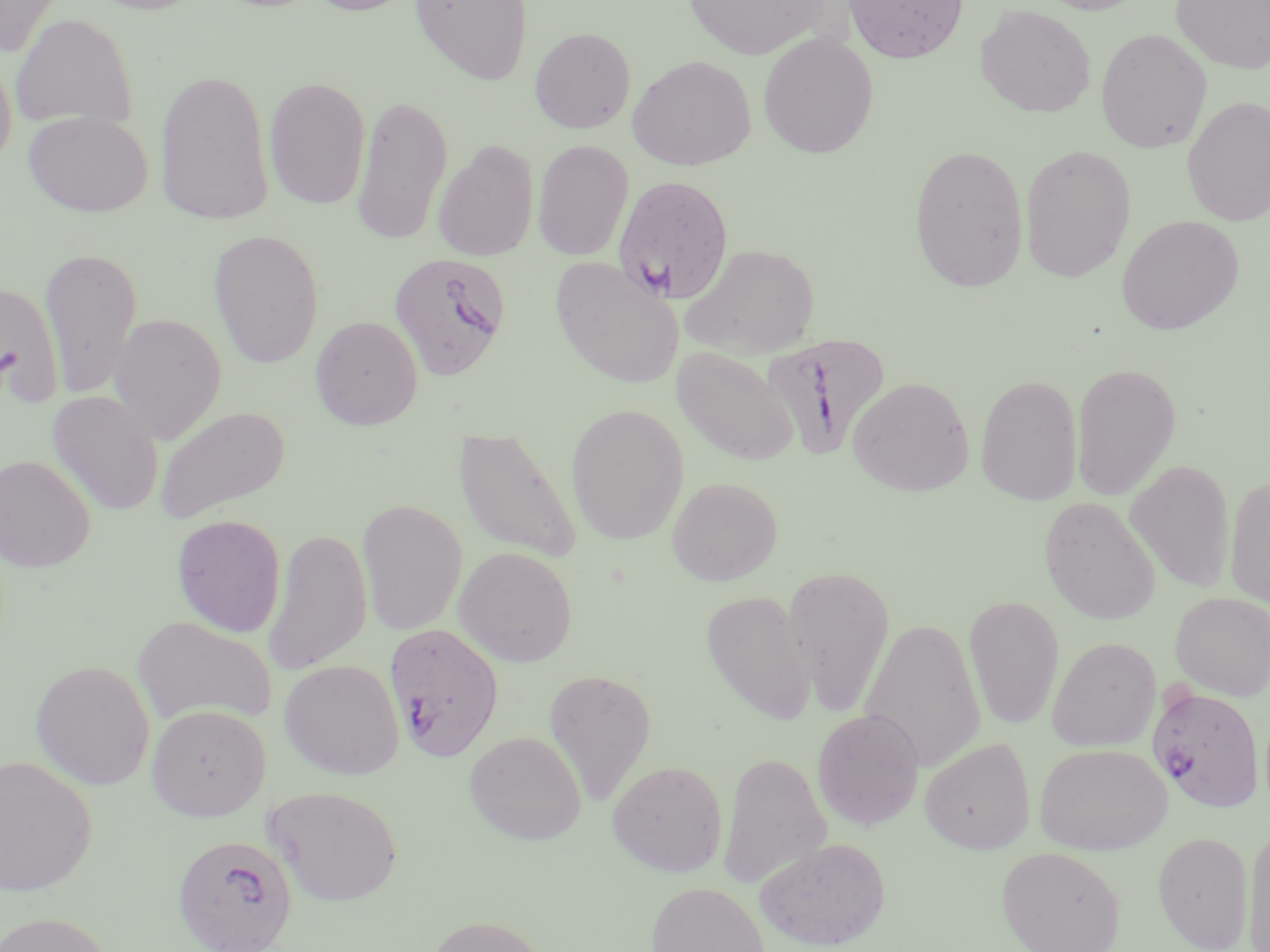
Summary:
  - Coordinate format: approximate bounding boxes as [x1, y1, x2, y2] in pixels
  - Uninfected red blood cell locations: [0, 0, 69, 55], [83, 0, 211, 15], [303, 0, 419, 16], [409, 0, 532, 86], [682, 0, 831, 61], [842, 0, 968, 64], [1033, 0, 1149, 15], [1169, 0, 1270, 74], [975, 4, 1096, 118], [10, 14, 137, 130], [529, 27, 636, 134], [1095, 28, 1212, 154], [757, 31, 879, 160], [0, 48, 17, 170], [627, 55, 757, 170], [154, 67, 275, 226], [264, 76, 371, 211], [351, 92, 453, 247], [1182, 95, 1270, 226], [23, 110, 154, 217], [433, 140, 539, 262], [533, 140, 633, 261], [908, 143, 1030, 293], [1019, 145, 1137, 282], [1116, 215, 1243, 334], [208, 228, 325, 368], [681, 243, 820, 358], [39, 245, 143, 400], [551, 256, 684, 390], [0, 280, 64, 407], [109, 313, 227, 444], [309, 315, 423, 430], [671, 345, 800, 467], [1071, 362, 1181, 502], [975, 373, 1083, 505], [847, 376, 974, 496], [47, 391, 164, 516], [566, 403, 689, 544], [153, 405, 292, 524], [454, 428, 582, 563], [0, 454, 96, 571], [1125, 459, 1235, 593], [1224, 474, 1270, 609], [666, 476, 783, 586], [1038, 496, 1160, 625], [357, 499, 467, 636], [171, 514, 287, 637], [263, 528, 372, 676], [454, 545, 578, 667], [782, 564, 897, 717], [700, 589, 817, 725], [1170, 592, 1270, 700], [964, 595, 1064, 730], [132, 615, 277, 727], [859, 618, 986, 772], [1047, 636, 1161, 752], [30, 659, 155, 790], [279, 659, 404, 779], [543, 667, 657, 804], [147, 704, 270, 821], [811, 708, 925, 830], [464, 731, 587, 845], [920, 737, 1036, 854], [1035, 742, 1172, 855], [718, 751, 831, 890], [1, 754, 97, 896], [607, 760, 728, 876], [264, 785, 403, 906], [1245, 825, 1270, 952], [1152, 831, 1254, 951], [755, 837, 891, 951], [996, 846, 1126, 952], [646, 882, 769, 952], [1, 910, 114, 952], [424, 914, 549, 952]
  - Plasmodium falciparum-infected red blood cell locations: [613, 175, 734, 304], [388, 252, 511, 379], [756, 335, 893, 459], [384, 622, 505, 762], [1147, 685, 1265, 813], [172, 835, 298, 951]
  - Slide-level diagnosis: Plasmodium falciparum
  - Image size: 1270×952 pixels
  - Magnification: 1000x
  - Preparation: thin blood smear
  - Stain: May-Grünwald-Giemsa
  - Modality: light microscopy
  - Field of view: single